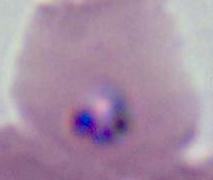

Summary:
  - Magnification: 400x or 1000x
  - Identification: Plasmodium
  - Modality: micrograph